Assess this cell for malaria.
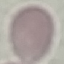
It is uninfected.

Summary:
  - Preparation: thin blood smear
  - Stain: Giemsa
  - Capture: smartphone camera at the microscope eyepiece
  - Image type: cell patch, automatically extracted from a larger field of view and resized to 64 × 64 pixels